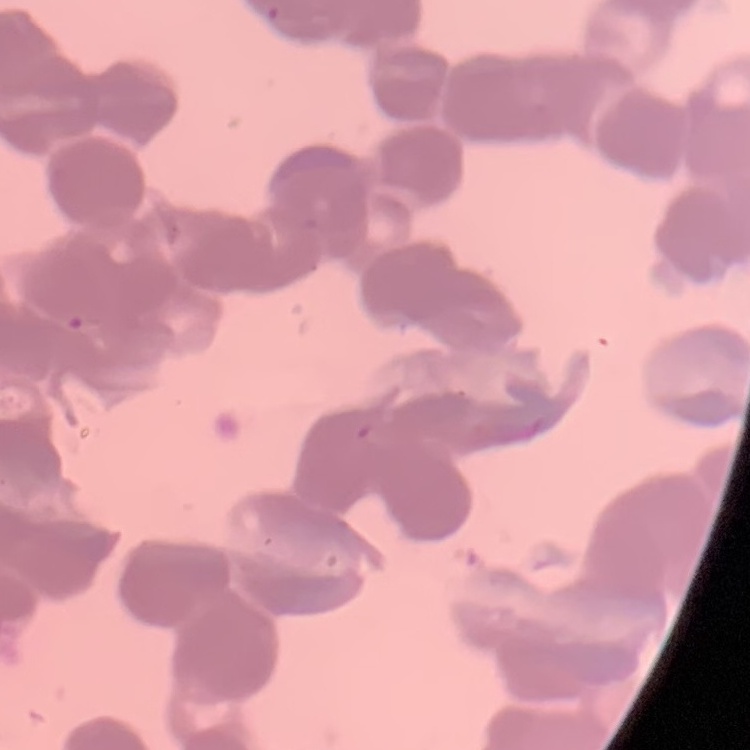
red_blood_cell_morphology: rouleaux formation
image_type: one tile cut from a larger photomicrograph
preparation: thin blood film
stain: Field's or Giemsa